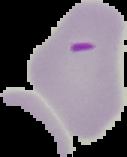

Summary:
  - Preparation: thin blood film
  - Image type: cell region segmented out of the field of view; surrounding area masked to black
  - Image size: 127×157 pixels
  - Result: Plasmodium parasites detected